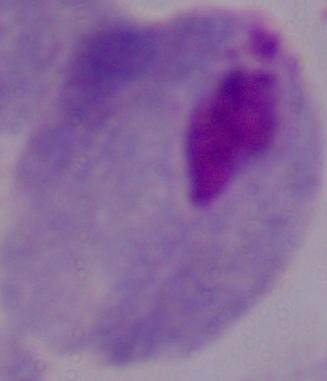
modality = photomicrograph
magnification = 1000x
identification = trichomonad